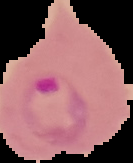

Summary:
  - Preparation: thin blood smear
  - Result: malaria parasites detected
  - Image type: segmented cell region on a black background
  - Image size: 133×163 pixels